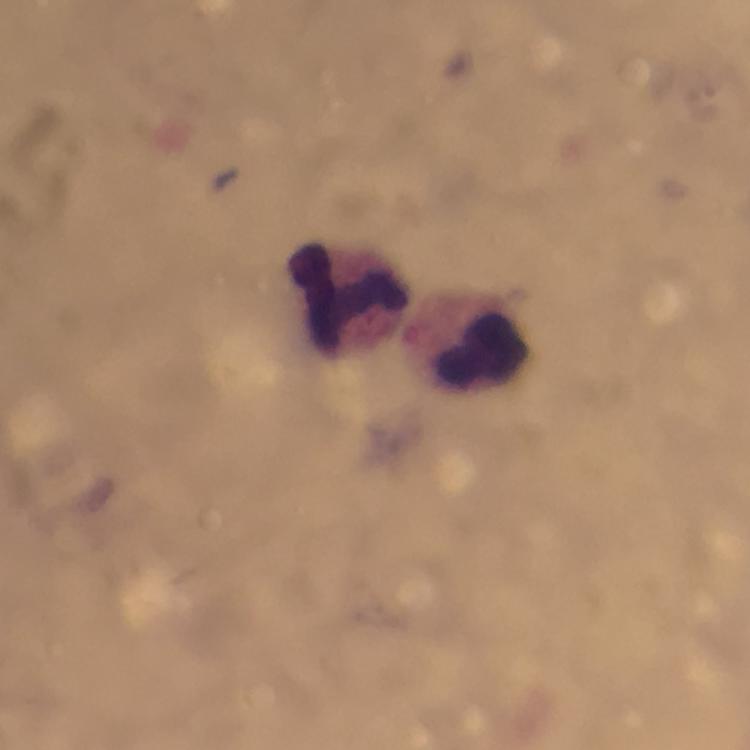
Approximate centers as (x, y) in pixels.
Summary:
  - Leukocyte locations: (346, 296), (480, 352)
  - Preparation: thick smear
  - Stain: Giemsa
  - Capture: smartphone mounted on the microscope
  - Image size: 750×750 pixels
  - Malaria parasites: none seen
  - Cropped from: a single field of view
  - Magnification: 100x
  - Context: from a malaria diagnostic workup
  - Immersion oil: used